Identify the blood parasite species.
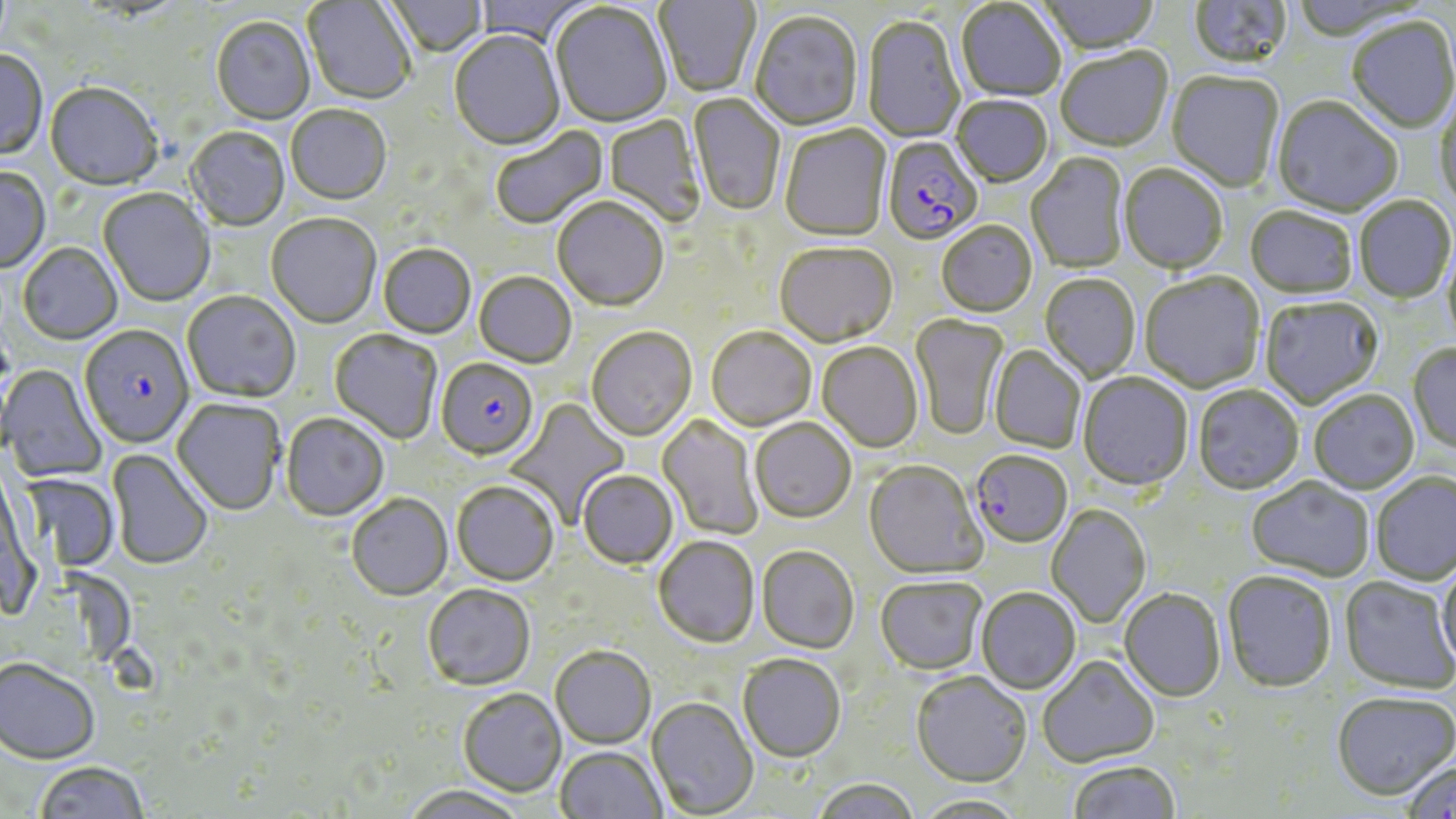

Plasmodium falciparum.

Approximate bounding boxes as [x1, y1, x2, y2] in pixels. Uninfected red blood cell locations: [383, 0, 488, 59], [473, 0, 593, 48], [654, 0, 760, 99], [1038, 0, 1159, 56], [1187, 0, 1292, 73], [303, 1, 415, 106], [956, 2, 1066, 103], [551, 4, 672, 129], [749, 13, 864, 133], [862, 17, 966, 144], [211, 18, 315, 126], [1347, 18, 1455, 135], [449, 31, 565, 152], [1056, 48, 1173, 154], [0, 51, 48, 162], [1166, 72, 1284, 194], [45, 84, 162, 192], [687, 93, 786, 217], [1434, 96, 1456, 211], [952, 97, 1053, 189], [1272, 99, 1403, 218], [286, 107, 391, 207], [604, 114, 706, 227], [491, 125, 608, 231], [779, 125, 892, 243], [186, 128, 289, 232], [1026, 153, 1129, 273], [1119, 165, 1228, 275], [0, 168, 51, 274], [98, 189, 215, 308], [1355, 197, 1455, 304], [552, 199, 669, 313], [1245, 208, 1357, 300], [265, 215, 381, 330], [936, 222, 1037, 318], [1443, 235, 1456, 355], [17, 244, 123, 345], [774, 244, 898, 350], [378, 246, 475, 340], [1140, 272, 1266, 394], [474, 273, 576, 370], [1040, 274, 1141, 382], [181, 292, 300, 404], [1260, 298, 1383, 410], [911, 314, 1009, 440], [706, 328, 817, 432], [586, 329, 697, 443], [329, 330, 442, 445], [817, 342, 924, 453], [1408, 344, 1456, 456], [989, 345, 1085, 454], [0, 365, 106, 483], [1077, 373, 1193, 492], [1193, 386, 1304, 496], [1309, 390, 1420, 495], [503, 398, 631, 527], [172, 399, 286, 517], [280, 414, 389, 522], [656, 414, 764, 540], [750, 419, 856, 525], [107, 449, 212, 571], [863, 462, 986, 580], [577, 471, 678, 570], [19, 473, 119, 572], [1370, 473, 1456, 586], [1246, 478, 1374, 582], [451, 482, 559, 587], [347, 495, 452, 601], [1045, 505, 1151, 628], [653, 537, 759, 649], [756, 548, 859, 655], [1437, 558, 1456, 671], [1223, 572, 1336, 694], [1339, 577, 1456, 695], [875, 578, 986, 676], [423, 585, 536, 691], [975, 588, 1080, 695], [1118, 590, 1225, 703], [551, 647, 656, 749], [738, 656, 846, 764], [1037, 657, 1159, 768], [0, 658, 100, 764], [911, 674, 1031, 789], [458, 689, 567, 798], [1331, 691, 1456, 800], [646, 697, 759, 818], [555, 747, 666, 819], [1400, 759, 1456, 819], [1069, 761, 1179, 819], [34, 762, 149, 819], [812, 779, 920, 819], [401, 785, 530, 819], [911, 795, 1028, 819]. Plasmodium falciparum-infected red blood cell locations: [882, 138, 984, 247], [79, 325, 194, 450], [436, 359, 538, 463], [969, 452, 1072, 549]. Thin blood smear. One field of a larger specimen. May-Grünwald-Giemsa stain. Image is 1456×819 pixels. Optical microscopy. 1000x magnification.